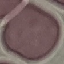

{
  "malaria_status": "uninfected",
  "preparation": "thin blood smear",
  "image_type": "cell patch, automatically extracted from a larger field of view and resized to 64 × 64 pixels",
  "stain": "Giemsa",
  "capture": "smartphone camera at the microscope eyepiece"
}